Give the extent of all Plasmodium falciparum-infected red blood cells.
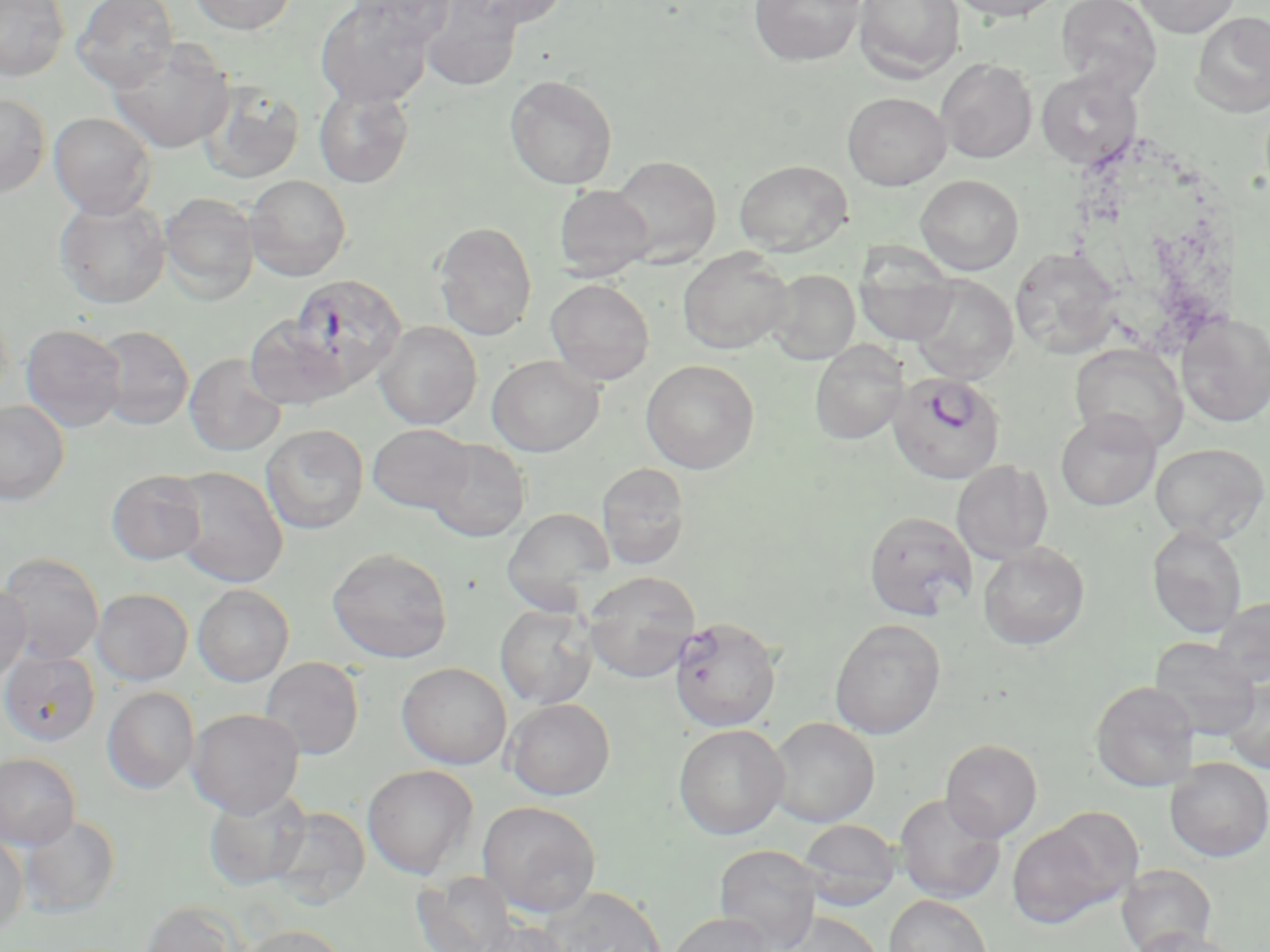

Approximate bounding boxes as [x1, y1, x2, y2] in pixels.
Plasmodium falciparum-infected red blood cells (subset): [289, 274, 407, 390].

{
  "slide_level_diagnosis": "Plasmodium falciparum",
  "modality": "light microscopy",
  "image_size": "1270×952 pixels",
  "magnification": "1000x",
  "field_of_view": "single",
  "uninfected_red_blood_cell_locations_subset": "approximate bounding boxes as [x1, y1, x2, y2] in pixels: [0, 0, 69, 81], [73, 0, 179, 91], [189, 0, 297, 34], [348, 0, 456, 45], [448, 0, 571, 32], [748, 0, 865, 66], [854, 0, 965, 81], [945, 0, 1066, 21], [1055, 0, 1162, 97], [1133, 0, 1240, 37], [316, 1, 433, 107], [419, 2, 523, 92], [1192, 11, 1270, 117], [107, 37, 234, 154], [936, 58, 1037, 164], [1036, 70, 1142, 169], [504, 75, 617, 190], [197, 81, 305, 184], [313, 86, 414, 188], [843, 92, 951, 190], [0, 93, 50, 196], [49, 112, 156, 218], [607, 154, 722, 266], [734, 160, 852, 256], [915, 174, 1024, 275], [244, 175, 351, 280], [554, 185, 653, 278], [160, 192, 259, 303], [55, 195, 171, 309], [434, 221, 537, 341], [1010, 247, 1121, 359], [678, 248, 793, 354], [855, 261, 959, 345], [765, 269, 860, 365], [909, 275, 1018, 384], [546, 278, 655, 385], [1177, 311, 1270, 428], [243, 315, 348, 409], [374, 321, 482, 430], [21, 324, 127, 432], [94, 325, 194, 430], [810, 340, 909, 444], [1070, 344, 1187, 453], [184, 353, 286, 456], [487, 355, 605, 457], [641, 359, 759, 473], [0, 400, 69, 504], [1055, 410, 1161, 511], [368, 423, 475, 514], [261, 424, 368, 534], [423, 438, 530, 542], [1150, 442, 1268, 544], [952, 460, 1053, 563], [596, 463, 690, 570], [169, 467, 288, 587], [106, 470, 207, 565], [502, 507, 615, 610], [864, 511, 977, 620], [1146, 525, 1248, 638], [977, 543, 1090, 650], [328, 546, 453, 663], [0, 552, 104, 665], [582, 571, 700, 683], [0, 583, 32, 683], [192, 584, 294, 686], [91, 588, 192, 685], [1209, 596, 1270, 688], [495, 603, 597, 709], [668, 616, 782, 732], [829, 619, 946, 739], [1149, 637, 1262, 739], [0, 650, 100, 746], [259, 657, 365, 760], [397, 662, 512, 769], [1221, 675, 1270, 775], [1089, 680, 1200, 792], [102, 687, 199, 794], [504, 697, 615, 800], [187, 708, 304, 817], [767, 717, 880, 828], [673, 723, 790, 840], [941, 739, 1042, 841], [0, 753, 81, 850], [1164, 757, 1269, 862], [362, 764, 479, 879], [203, 785, 311, 891], [894, 793, 1006, 904], [477, 800, 601, 917], [1039, 805, 1146, 913], [267, 806, 370, 908], [19, 814, 120, 917], [798, 819, 901, 910], [1007, 821, 1115, 928], [0, 832, 28, 936], [714, 844, 823, 951], [1116, 863, 1217, 952], [411, 871, 517, 952], [536, 886, 668, 951], [884, 894, 994, 952], [140, 900, 246, 952], [779, 910, 886, 952], [666, 912, 777, 952], [473, 918, 573, 952], [240, 924, 346, 952], [1130, 927, 1247, 952]",
  "preparation": "thin blood smear",
  "stain": "May-Grünwald-Giemsa"
}